Outline each uninfected red blood cell.
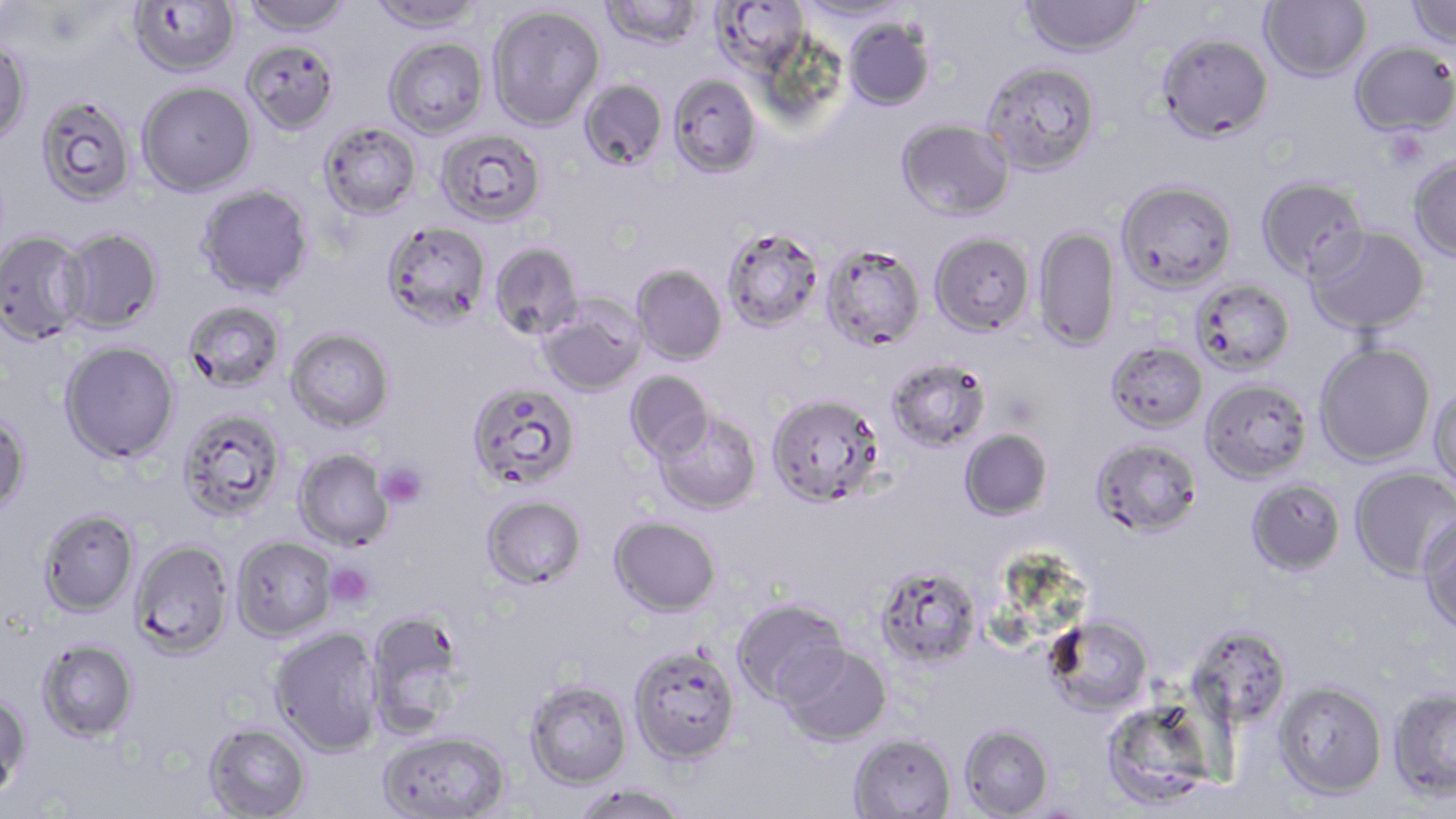
Approximate bounding boxes as (x1,y1)-(x2,y2) corner pairs in pixels.
Uninfected red blood cells: (128,0)-(241,76), (242,0)-(353,35), (368,0)-(484,35), (600,0)-(703,51), (712,0)-(809,74), (794,0)-(911,23), (1021,0)-(1145,57), (1259,0)-(1371,82), (1406,0)-(1456,50), (488,5)-(605,130), (844,18)-(935,110), (1156,32)-(1274,142), (241,38)-(339,134), (384,38)-(489,138), (0,39)-(32,147), (1350,40)-(1456,137), (981,60)-(1101,176), (668,73)-(762,177), (578,79)-(667,170), (137,82)-(256,196), (35,96)-(137,206), (897,118)-(1014,221), (318,122)-(422,220), (436,129)-(546,227), (1408,154)-(1456,261), (1255,175)-(1368,281), (1116,179)-(1238,293), (197,185)-(314,298), (382,221)-(490,330), (1305,225)-(1430,336), (721,226)-(824,333), (1033,226)-(1120,351), (59,228)-(163,333), (0,230)-(89,344), (930,232)-(1035,335), (489,242)-(584,340), (821,243)-(925,351), (631,265)-(727,364), (1191,278)-(1295,375), (538,298)-(646,397), (182,301)-(285,392), (286,329)-(394,432), (59,341)-(180,463), (1314,341)-(1437,467), (1105,342)-(1208,433), (886,357)-(991,452), (625,370)-(714,461), (1200,378)-(1313,483), (467,382)-(580,491), (1429,384)-(1456,493), (766,393)-(885,507), (177,410)-(286,520), (653,410)-(762,514), (0,412)-(31,516), (959,429)-(1053,521), (1091,438)-(1203,538), (294,449)-(394,550), (1349,466)-(1456,581), (1245,478)-(1346,577), (481,494)-(587,589), (37,508)-(140,617), (1417,514)-(1456,634), (609,515)-(721,617), (232,535)-(337,640), (130,539)-(234,658), (873,564)-(983,670), (732,597)-(850,707), (366,610)-(470,736), (1043,614)-(1154,717), (1186,625)-(1293,729), (269,627)-(383,756), (36,638)-(138,742), (628,644)-(741,764), (779,644)-(892,746), (524,680)-(632,789), (1273,681)-(1388,799), (1388,689)-(1456,799), (0,690)-(32,801), (1106,710)-(1209,808), (203,722)-(310,818), (959,724)-(1054,818), (377,730)-(510,818), (849,733)-(957,818), (572,783)-(690,819).

Platelet locations: (376,462)-(427,508), (326,563)-(376,609). Slide-level diagnosis: Plasmodium falciparum. Single field of view. 1000x magnification. May-Grünwald-Giemsa-stained preparation. Light microscopy. Image is 1456×819 pixels. Thin blood film.